Assess this cell for malaria.
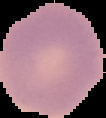
It is uninfected.

image type = segmented cell region with the area outside set to black
image size = 106×118 pixels
preparation = thin blood film